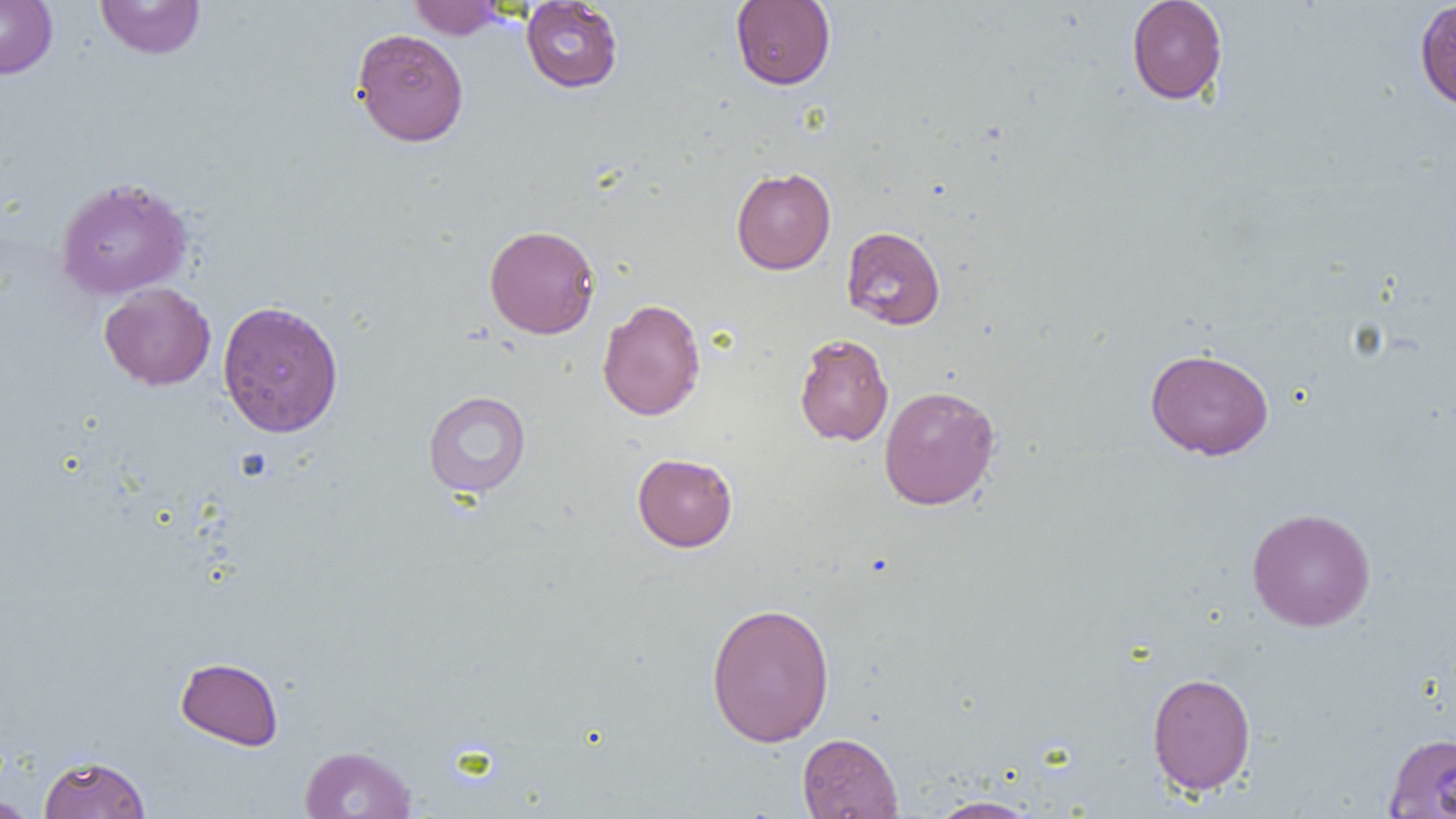

Summary:
  - Coordinate format: approximate bounding boxes as (x1,y1)-(x2,y2) corner pairs in pixels
  - Uninfected red blood cell locations: (0,0)-(57,79), (95,0)-(206,59), (408,0)-(507,39), (521,0)-(623,93), (730,0)-(836,90), (1126,0)-(1228,105), (1414,0)-(1456,111), (351,28)-(469,146), (731,167)-(836,274), (54,177)-(192,300), (484,224)-(600,339), (841,225)-(946,330), (99,282)-(216,390), (597,299)-(706,421), (217,300)-(344,438), (793,333)-(894,446), (1145,348)-(1274,460), (878,385)-(1000,510), (422,391)-(531,498), (632,453)-(738,552), (1246,507)-(1376,632), (705,602)-(835,747), (175,657)-(284,750), (1147,671)-(1256,795), (797,732)-(904,818), (1383,732)-(1456,817), (299,744)-(416,819), (38,754)-(151,818), (0,795)-(39,819), (926,795)-(1042,818)
  - Slide-level diagnosis: negative for blood parasites
  - Modality: light microscopy
  - Image size: 1456×819 pixels
  - Magnification: 1000x
  - Preparation: thin blood film
  - Field of view: single